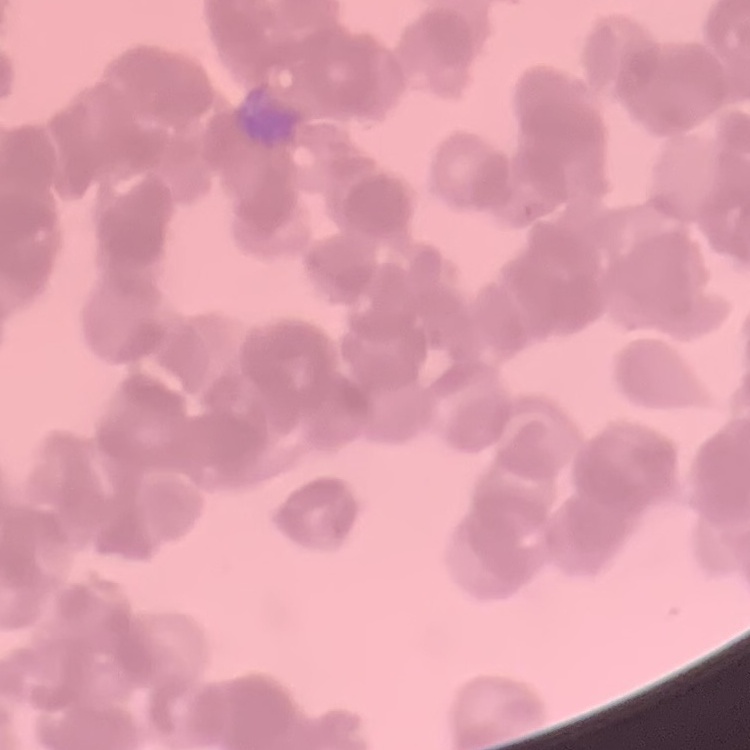
The red blood cells exhibit rouleaux formation. Thin blood film. One tile cut from a larger photomicrograph. Field's or Giemsa stain.